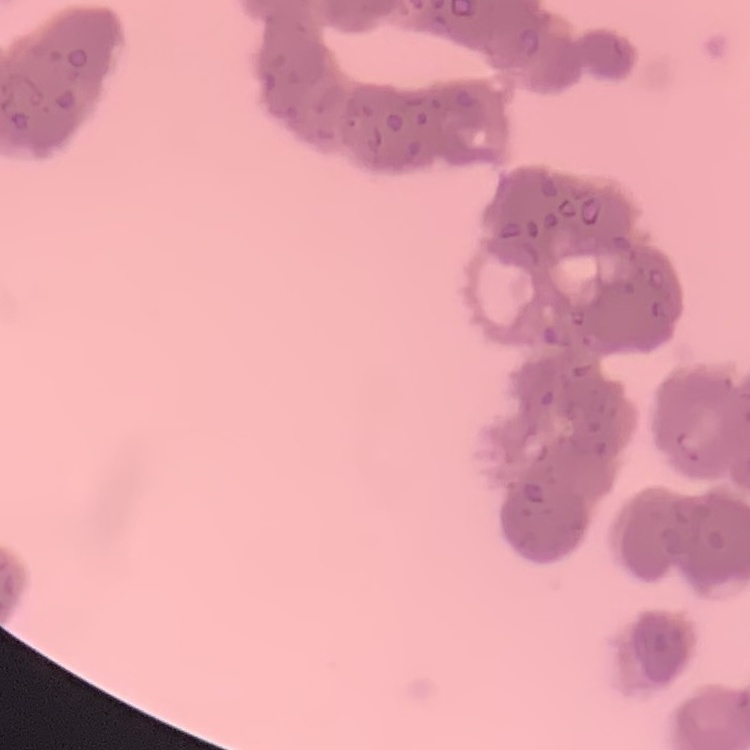
{
  "erythrocyte_morphology": "rouleaux formation",
  "stain": "Field's or Giemsa",
  "preparation": "thin blood film",
  "image_type": "square crop of a larger photomicrograph"
}